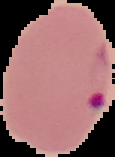

Summary:
  - Preparation: thin blood smear
  - Image type: segmented cell region on a black background
  - Image size: 115×157 pixels
  - Malaria status: parasitized